Identify the preparation type.
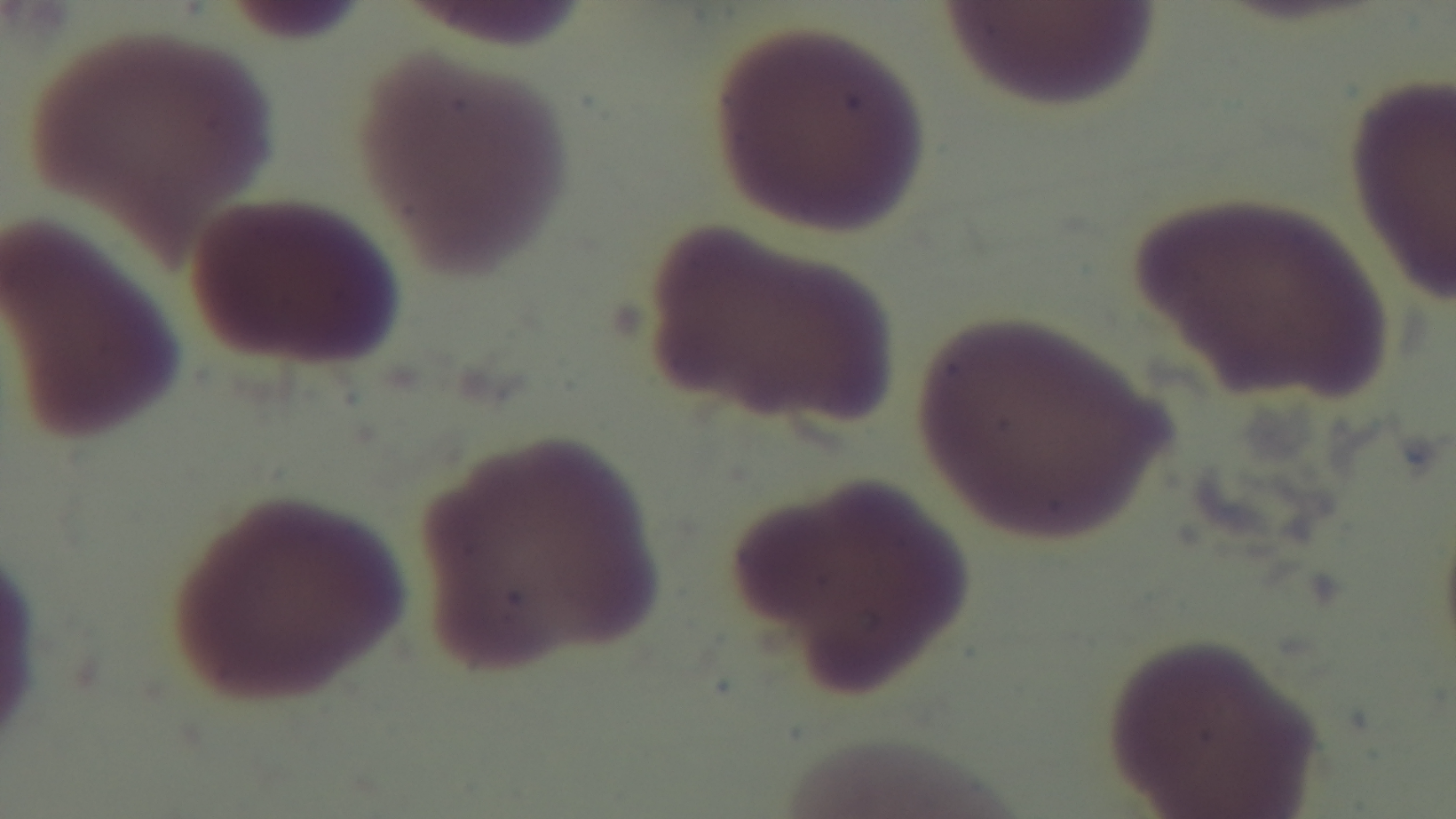

A thin smear.

Mounted 4K digital camera. Light microscopy. Malaria status: uninfected. Oil-immersion objective, 100x. Single field of view. Giemsa-stained.